Point out each malaria parasite.
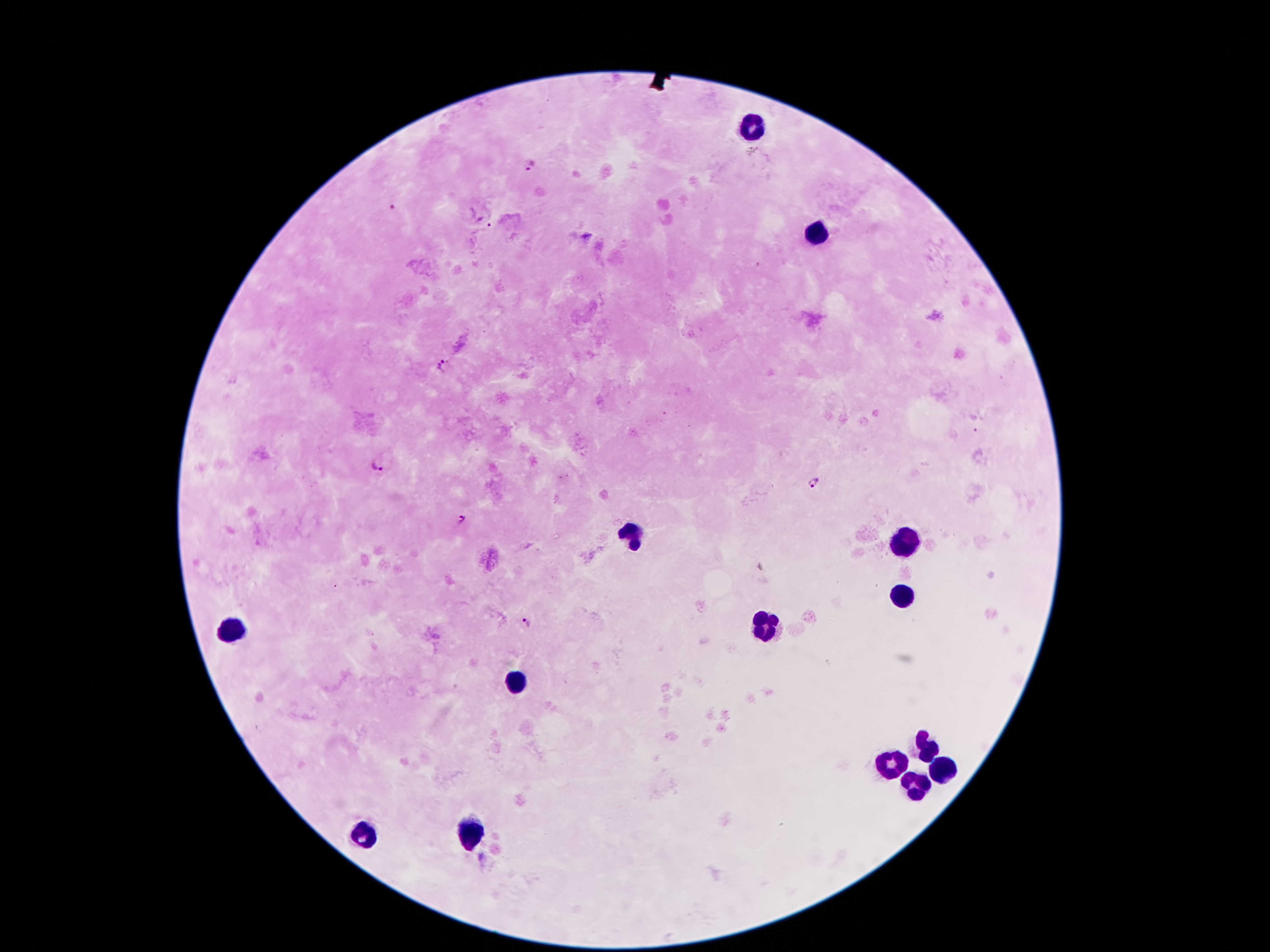
Approximate centers as [x, y] in pixels.
Malaria parasites: [529, 165], [395, 206], [488, 227], [443, 365], [377, 463], [814, 485], [460, 521], [527, 623].

Leukocyte locations: [753, 128], [812, 232], [631, 536], [905, 543], [903, 598], [765, 627], [231, 629], [515, 679], [926, 747], [894, 766], [939, 768], [917, 784], [469, 831], [365, 836]. Single field of view. Giemsa-stained preparation. Patient malaria status: positive for Plasmodium falciparum. 100x magnification. Thick peripheral-blood smear. Image is 1270×952 pixels. Smartphone photograph taken through the microscope eyepiece.